Identify the cell.
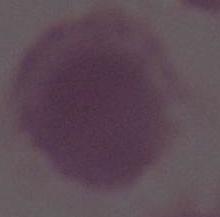
An erythrocyte.

Summary:
  - Magnification: 1000x
  - Modality: photomicrograph